Classify this cell by malaria status.
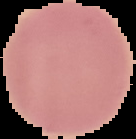
Uninfected.

Image is 136×139 pixels. From a thin blood film. Cell region segmented out of the field of view; the surrounding area is masked to black.